Name the parasite shown.
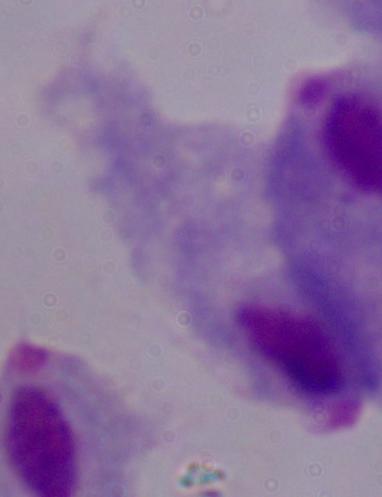
A trichomonad.

Photomicrograph. Captured at 1000x magnification.